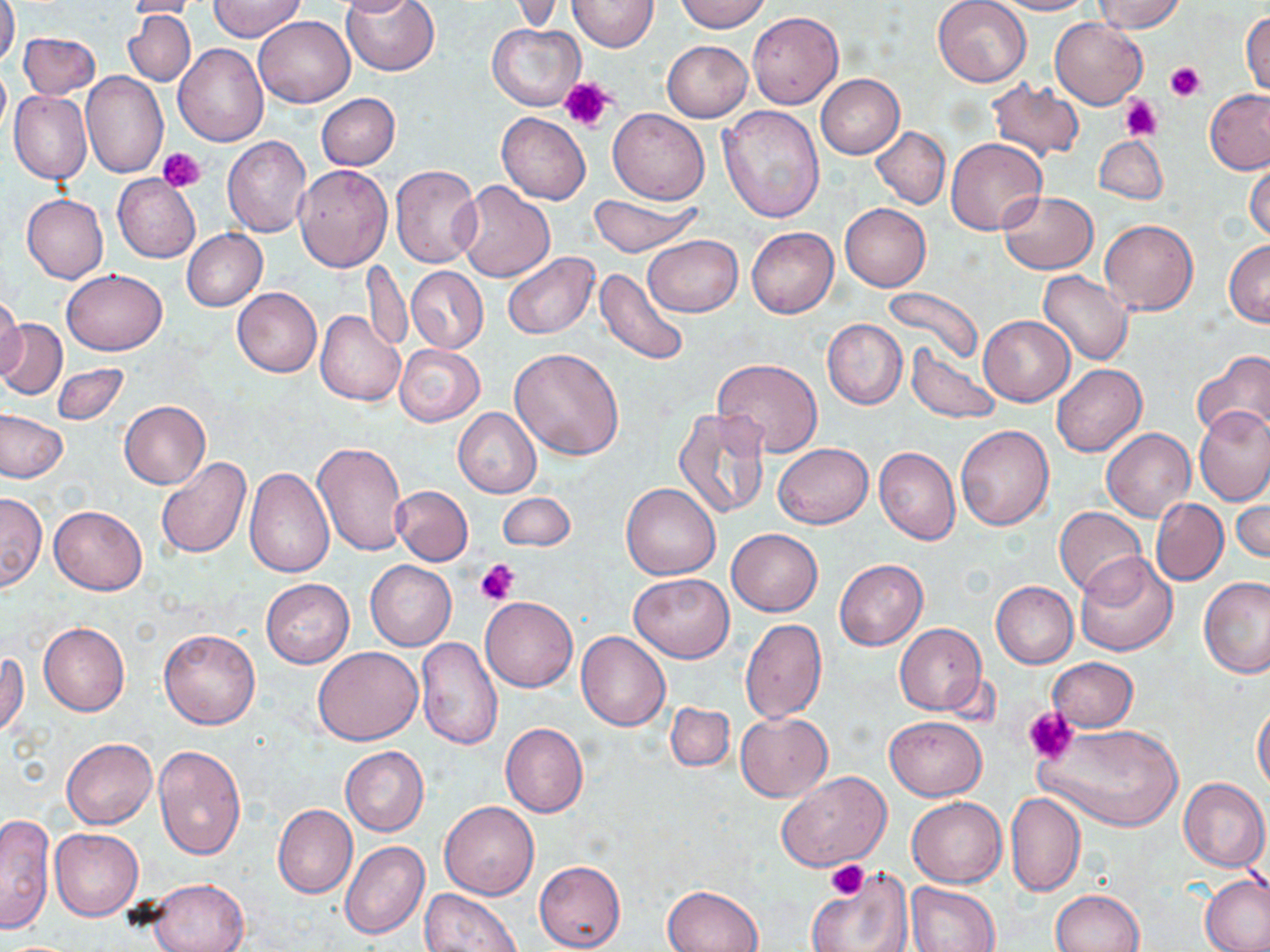

slide-level diagnosis = negative for blood parasites
uninfected red blood cell locations = approximate bounding boxes as named x1/y1/x2/y2 corners in pixels: (x1=0, y1=0, x2=20, y2=69), (x1=124, y1=0, x2=212, y2=19), (x1=210, y1=0, x2=305, y2=41), (x1=333, y1=0, x2=422, y2=16), (x1=340, y1=0, x2=439, y2=76), (x1=568, y1=0, x2=659, y2=51), (x1=677, y1=0, x2=768, y2=32), (x1=932, y1=0, x2=1031, y2=86), (x1=993, y1=0, x2=1092, y2=15), (x1=1094, y1=0, x2=1184, y2=33), (x1=123, y1=11, x2=196, y2=87), (x1=748, y1=11, x2=844, y2=109), (x1=1242, y1=11, x2=1270, y2=98), (x1=254, y1=14, x2=355, y2=107), (x1=1050, y1=18, x2=1147, y2=109), (x1=487, y1=22, x2=585, y2=111), (x1=19, y1=32, x2=100, y2=101), (x1=662, y1=41, x2=752, y2=121), (x1=174, y1=43, x2=269, y2=146), (x1=0, y1=64, x2=10, y2=139), (x1=80, y1=70, x2=168, y2=178), (x1=815, y1=74, x2=904, y2=159), (x1=987, y1=79, x2=1085, y2=162), (x1=1205, y1=89, x2=1270, y2=175), (x1=9, y1=91, x2=92, y2=184), (x1=317, y1=93, x2=400, y2=170), (x1=717, y1=105, x2=824, y2=224), (x1=608, y1=108, x2=709, y2=204), (x1=497, y1=111, x2=591, y2=205), (x1=869, y1=126, x2=950, y2=209), (x1=1094, y1=135, x2=1168, y2=205), (x1=222, y1=136, x2=311, y2=237), (x1=945, y1=137, x2=1046, y2=235), (x1=1245, y1=157, x2=1270, y2=244), (x1=293, y1=164, x2=391, y2=271), (x1=390, y1=164, x2=482, y2=268), (x1=113, y1=173, x2=200, y2=263), (x1=453, y1=183, x2=555, y2=283), (x1=999, y1=191, x2=1098, y2=274), (x1=588, y1=193, x2=701, y2=257), (x1=21, y1=194, x2=108, y2=283), (x1=839, y1=204, x2=931, y2=291), (x1=1100, y1=218, x2=1198, y2=315), (x1=746, y1=227, x2=838, y2=317), (x1=182, y1=229, x2=266, y2=310), (x1=643, y1=235, x2=743, y2=317), (x1=1224, y1=241, x2=1270, y2=326), (x1=503, y1=251, x2=599, y2=340), (x1=362, y1=259, x2=413, y2=354), (x1=407, y1=266, x2=488, y2=353), (x1=594, y1=268, x2=691, y2=366), (x1=61, y1=269, x2=168, y2=355), (x1=1039, y1=271, x2=1134, y2=367), (x1=880, y1=286, x2=983, y2=367), (x1=231, y1=287, x2=322, y2=378), (x1=0, y1=293, x2=26, y2=379), (x1=315, y1=310, x2=405, y2=406), (x1=978, y1=314, x2=1075, y2=406), (x1=822, y1=318, x2=907, y2=410), (x1=0, y1=319, x2=66, y2=399), (x1=394, y1=344, x2=486, y2=426), (x1=906, y1=345, x2=1001, y2=423), (x1=509, y1=347, x2=624, y2=460), (x1=1192, y1=350, x2=1270, y2=438), (x1=713, y1=358, x2=823, y2=458), (x1=53, y1=363, x2=129, y2=424), (x1=1052, y1=363, x2=1147, y2=456), (x1=120, y1=400, x2=210, y2=489), (x1=453, y1=407, x2=541, y2=498), (x1=673, y1=408, x2=773, y2=519), (x1=1194, y1=408, x2=1270, y2=505), (x1=1, y1=411, x2=66, y2=481), (x1=955, y1=425, x2=1054, y2=531), (x1=1102, y1=428, x2=1195, y2=521), (x1=314, y1=440, x2=408, y2=557), (x1=773, y1=443, x2=872, y2=529), (x1=873, y1=445, x2=960, y2=545), (x1=155, y1=457, x2=251, y2=558), (x1=244, y1=466, x2=334, y2=577), (x1=621, y1=484, x2=720, y2=580), (x1=392, y1=485, x2=473, y2=565), (x1=1232, y1=487, x2=1269, y2=567), (x1=0, y1=492, x2=47, y2=591), (x1=498, y1=492, x2=574, y2=551), (x1=1151, y1=498, x2=1228, y2=586), (x1=50, y1=506, x2=147, y2=595), (x1=1054, y1=506, x2=1146, y2=596), (x1=727, y1=528, x2=822, y2=616), (x1=1074, y1=551, x2=1177, y2=655), (x1=835, y1=559, x2=928, y2=650), (x1=365, y1=560, x2=456, y2=651), (x1=630, y1=573, x2=734, y2=662), (x1=1198, y1=576, x2=1269, y2=679), (x1=260, y1=579, x2=354, y2=668), (x1=991, y1=581, x2=1078, y2=668), (x1=480, y1=597, x2=577, y2=693), (x1=740, y1=619, x2=827, y2=723), (x1=38, y1=621, x2=129, y2=718), (x1=894, y1=623, x2=987, y2=715), (x1=159, y1=628, x2=261, y2=729), (x1=576, y1=630, x2=670, y2=731), (x1=416, y1=638, x2=502, y2=750), (x1=313, y1=645, x2=422, y2=744), (x1=1, y1=650, x2=28, y2=738), (x1=1047, y1=657, x2=1138, y2=732), (x1=664, y1=701, x2=734, y2=771), (x1=1253, y1=702, x2=1270, y2=792), (x1=736, y1=713, x2=832, y2=801), (x1=884, y1=716, x2=985, y2=800), (x1=1035, y1=721, x2=1184, y2=832), (x1=500, y1=722, x2=588, y2=817), (x1=61, y1=737, x2=157, y2=829), (x1=153, y1=745, x2=246, y2=859), (x1=340, y1=745, x2=429, y2=835), (x1=777, y1=771, x2=892, y2=871), (x1=1179, y1=778, x2=1270, y2=872), (x1=1004, y1=791, x2=1085, y2=896), (x1=907, y1=797, x2=1006, y2=888), (x1=440, y1=802, x2=539, y2=900), (x1=273, y1=805, x2=357, y2=899), (x1=0, y1=812, x2=56, y2=935), (x1=50, y1=828, x2=143, y2=921), (x1=339, y1=840, x2=430, y2=940), (x1=534, y1=859, x2=625, y2=952), (x1=806, y1=866, x2=910, y2=952), (x1=1198, y1=873, x2=1270, y2=952), (x1=148, y1=879, x2=251, y2=952), (x1=905, y1=882, x2=999, y2=952), (x1=663, y1=885, x2=763, y2=952), (x1=420, y1=889, x2=520, y2=952), (x1=1052, y1=889, x2=1144, y2=952)
modality = light microscopy
field of view = single
platelet locations = approximate bounding boxes as named x1/y1/x2/y2 corners in pixels: (x1=1166, y1=62, x2=1206, y2=101), (x1=559, y1=75, x2=615, y2=133), (x1=1119, y1=97, x2=1162, y2=140), (x1=158, y1=147, x2=207, y2=192), (x1=476, y1=559, x2=520, y2=605), (x1=1023, y1=706, x2=1077, y2=763), (x1=826, y1=860, x2=869, y2=900)
magnification = 1000x
stain = May-Grünwald-Giemsa
preparation = thin blood film
image size = 1270×952 pixels